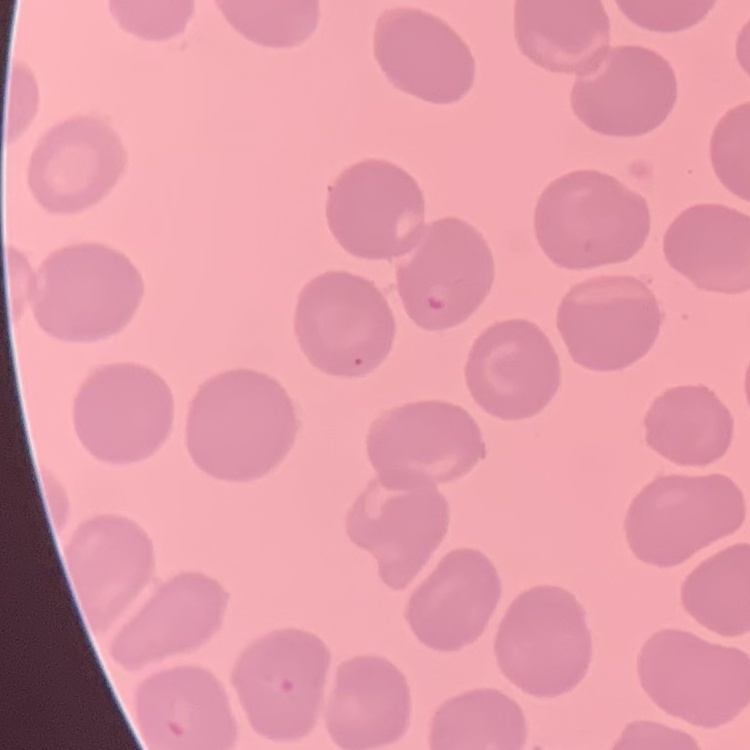
The red blood cells show no rouleaux formation. Square crop of a larger photomicrograph. Thin peripheral smear. Field's or Giemsa stain.